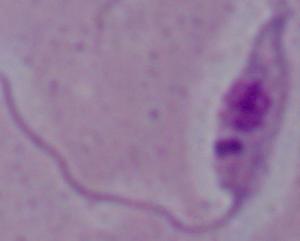

magnification = 1000x
modality = photomicrograph
identification = Leishmania